Report the malaria status of this cell.
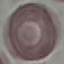

Uninfected.

Summary:
  - Preparation: thin blood film
  - Stain: Giemsa
  - Capture: smartphone camera at the microscope eyepiece
  - Image type: automatically extracted cell patch, resized to 64 × 64 pixels